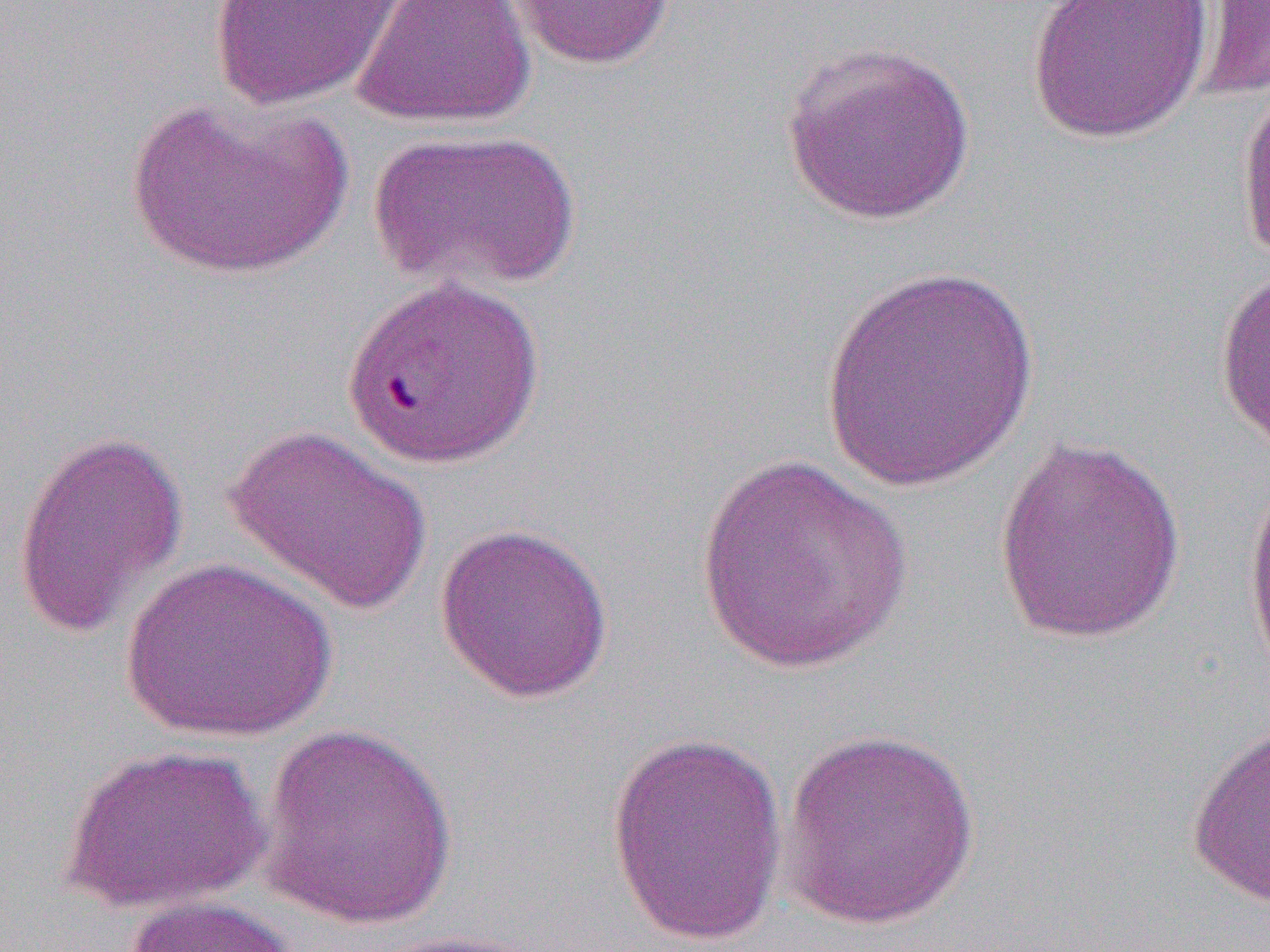
slide_level_diagnosis: Plasmodium falciparum
uninfected_red_blood_cell_locations_subset: 'approximate bounding boxes as (x1,y1)-(x2,y2) corner pairs in pixels: (207,0)-(409,110), (352,0)-(536,130), (503,0)-(682,70), (1025,0)-(1214,144), (1197,0)-(1270,102), (781,39)-(977,226), (1235,78)-(1270,271), (126,95)-(352,280), (366,128)-(580,293), (1214,259)-(1270,455), (817,265)-(1043,493), (223,423)-(432,618), (12,428)-(190,639), (992,435)-(1188,645), (691,452)-(916,673), (1241,465)-(1270,686), (433,522)-(615,703), (120,557)-(337,742), (255,722)-(460,929), (1186,722)-(1270,908), (778,728)-(984,931), (604,732)-(788,946), (59,743)-(271,916), (121,895)-(305,952)'
field_of_view: single
modality: light microscopy
magnification: 1000x
image_size: 1270×952 pixels
preparation: thin blood film